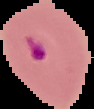

Malaria status: parasitized. Image is 94×109 pixels. From a thin blood smear. Cell region segmented out of the field of view; the surrounding area is masked to black.